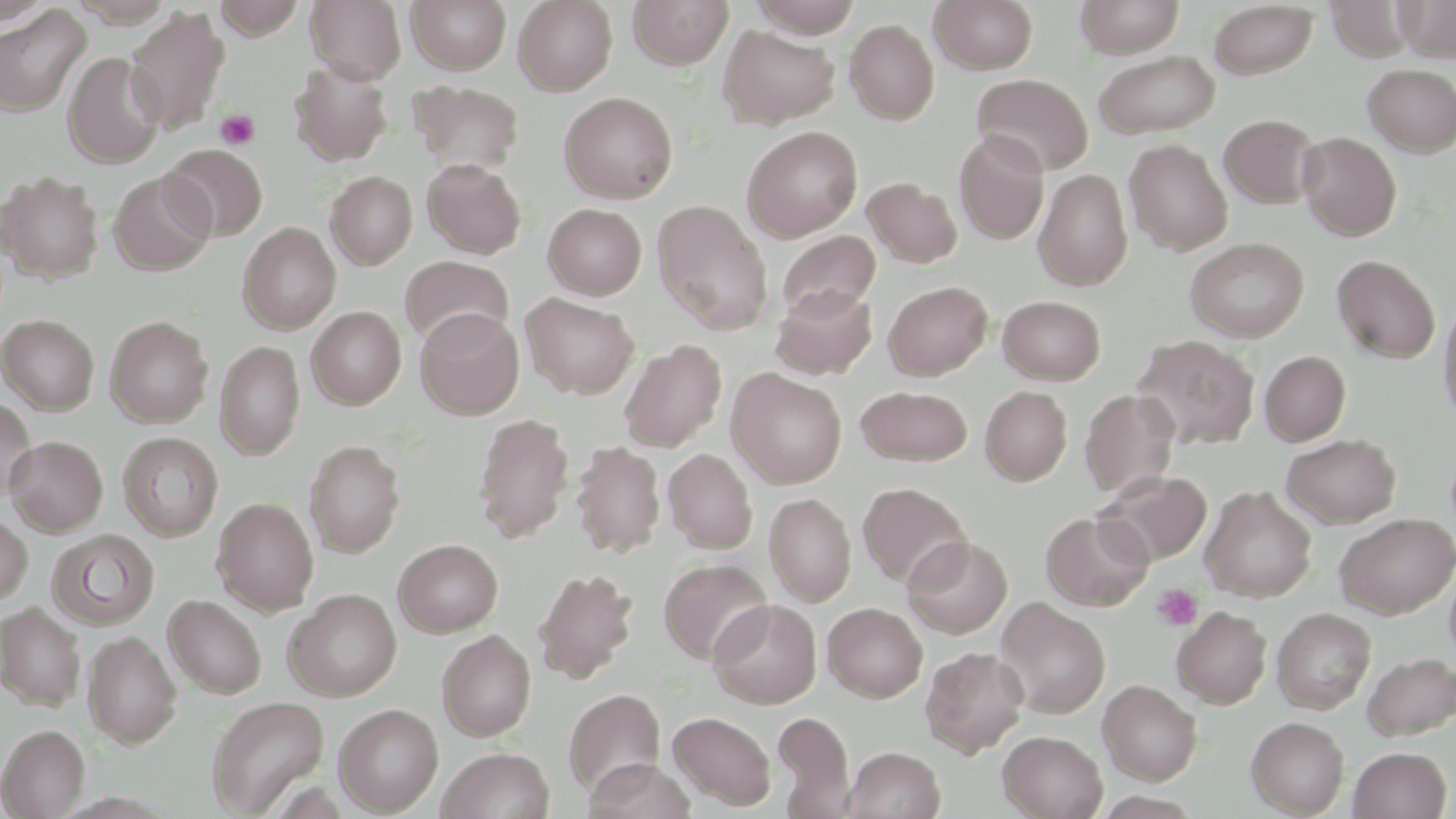
Approximate bounding boxes as (x1,y1)-(x2,y2) corner pairs in pixels. Platelet locations: (214,109)-(261,151), (1152,583)-(1202,631). Uninfected red blood cell locations: (212,0)-(307,40), (306,0)-(406,83), (407,0)-(511,74), (514,0)-(617,95), (627,0)-(733,69), (748,0)-(864,37), (930,0)-(1038,74), (1075,0)-(1184,58), (1326,0)-(1415,61), (1395,0)-(1456,61), (1209,2)-(1318,78), (0,5)-(90,117), (125,7)-(230,136), (845,19)-(939,124), (718,24)-(840,128), (1093,49)-(1220,139), (62,51)-(166,169), (289,61)-(393,166), (1362,63)-(1456,156), (971,73)-(1093,176), (409,80)-(524,179), (559,92)-(678,203), (1219,114)-(1319,208), (742,125)-(863,242), (954,129)-(1050,245), (1297,131)-(1401,241), (1125,139)-(1233,254), (164,144)-(268,241), (422,159)-(526,258), (1034,169)-(1133,290), (108,170)-(216,275), (1,171)-(103,282), (326,171)-(417,269), (863,177)-(962,268), (652,199)-(774,335), (543,203)-(647,300), (238,222)-(341,333), (775,230)-(881,325), (1185,237)-(1309,342), (1332,254)-(1440,364), (401,256)-(514,348), (883,280)-(993,380), (772,284)-(877,380), (521,293)-(639,399), (997,295)-(1106,385), (1438,297)-(1456,426), (306,306)-(405,409), (415,308)-(524,419), (1,315)-(99,413), (105,315)-(213,427), (1133,335)-(1259,449), (620,339)-(727,453), (215,340)-(305,459), (1260,350)-(1351,445), (727,369)-(847,488), (856,386)-(973,466), (980,386)-(1072,485), (1079,388)-(1182,499), (0,397)-(37,501), (473,412)-(574,543), (118,432)-(223,541), (1281,433)-(1401,528), (5,435)-(108,535), (304,440)-(404,557), (571,441)-(665,557), (663,448)-(757,554), (1095,469)-(1212,566), (858,482)-(971,589), (1200,486)-(1316,602), (765,492)-(856,606), (211,497)-(319,614), (1041,511)-(1153,611), (1334,513)-(1455,619), (0,514)-(33,606), (46,529)-(160,631), (903,535)-(1013,638), (394,539)-(503,637), (659,558)-(772,665), (1444,563)-(1456,666), (532,567)-(639,684), (283,589)-(402,701), (164,594)-(267,699), (995,598)-(1110,718), (708,599)-(822,708), (823,602)-(927,702), (0,603)-(86,710), (1172,605)-(1271,708), (1272,607)-(1376,714), (437,629)-(536,741), (82,630)-(182,748), (920,646)-(1030,757), (1361,652)-(1456,741), (1098,679)-(1202,785), (564,688)-(665,797), (205,695)-(329,817), (333,703)-(444,816), (668,711)-(776,810), (772,711)-(853,815), (1246,716)-(1349,817), (0,723)-(90,818), (998,730)-(1107,818), (436,747)-(555,819), (843,747)-(945,819), (1348,747)-(1452,819), (584,757)-(696,819). Slide-level diagnosis: no evidence of blood parasites. Thin blood film. May-Grünwald-Giemsa-stained preparation. Light microscopy. Image is 1456×819 pixels. Single field of view. 1000x magnification.